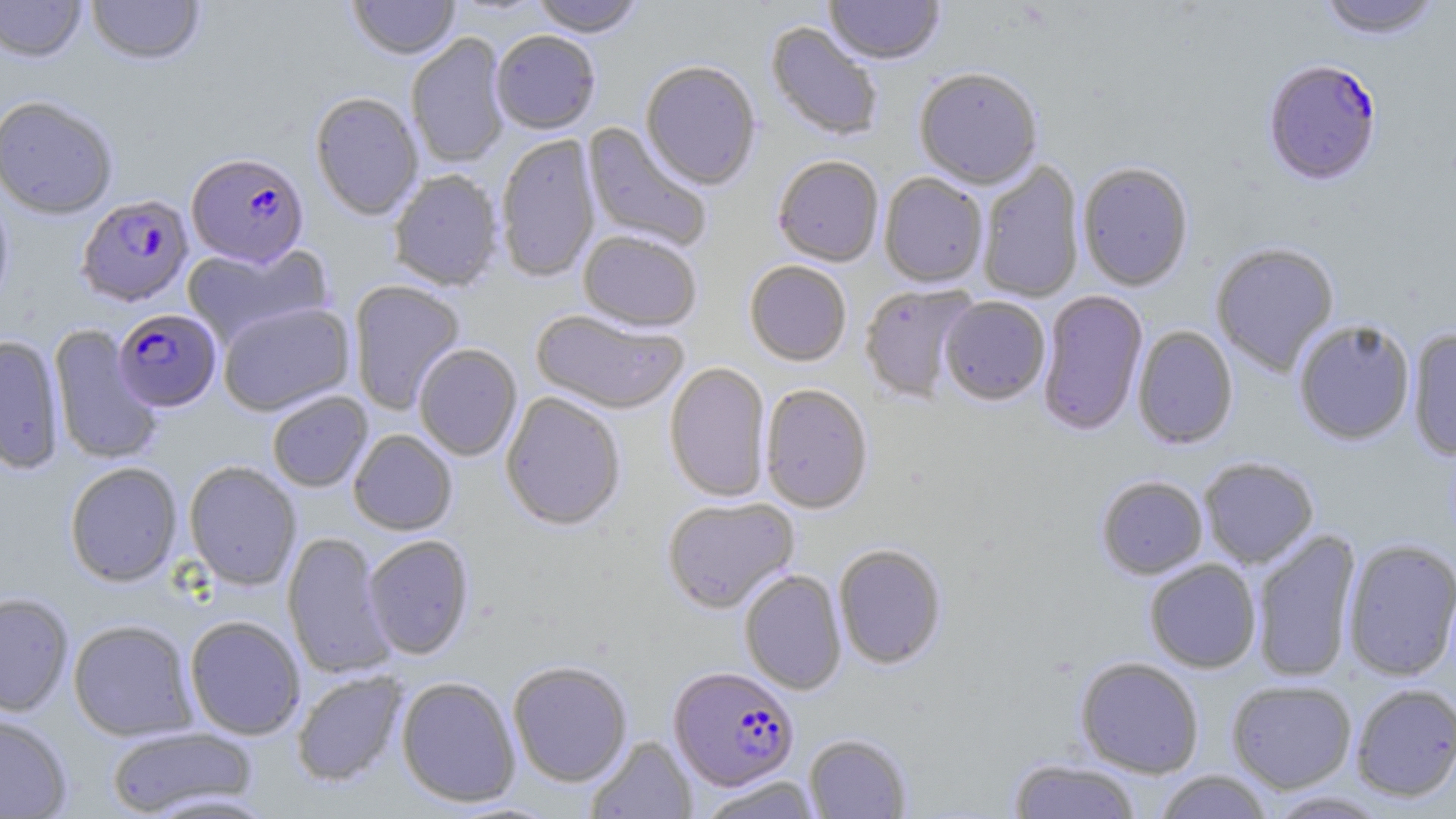 Approximate bounding boxes as (x1, y1, x2, y2) in pixels. Uninfected red blood cell locations: (0, 0, 88, 62), (85, 0, 205, 67), (347, 0, 461, 60), (530, 0, 646, 37), (825, 0, 944, 66), (1315, 0, 1445, 40), (765, 21, 884, 142), (490, 30, 601, 135), (406, 33, 510, 169), (640, 61, 761, 190), (913, 69, 1043, 189), (310, 92, 423, 221), (0, 94, 120, 220), (582, 122, 712, 253), (495, 134, 600, 283), (773, 156, 884, 267), (977, 159, 1084, 303), (1077, 161, 1194, 291), (388, 169, 504, 291), (879, 173, 988, 287), (0, 182, 14, 319), (578, 230, 702, 333), (1211, 242, 1340, 376), (182, 243, 332, 348), (744, 260, 852, 366), (348, 280, 466, 415), (859, 283, 977, 403), (1037, 290, 1148, 435), (939, 296, 1051, 405), (217, 301, 355, 415), (528, 309, 689, 416), (1293, 318, 1416, 445), (48, 325, 162, 465), (1132, 325, 1238, 450), (1407, 328, 1456, 462), (0, 335, 66, 474), (414, 344, 522, 461), (664, 362, 771, 503), (759, 383, 873, 514), (267, 391, 373, 492), (500, 391, 626, 530), (348, 429, 457, 535), (1198, 456, 1319, 567), (64, 461, 183, 587), (183, 461, 302, 590), (1096, 475, 1208, 579), (662, 496, 799, 613), (1250, 528, 1362, 683), (282, 531, 396, 680), (363, 535, 474, 660), (1342, 538, 1456, 681), (833, 543, 947, 670), (1144, 559, 1261, 673), (739, 569, 847, 695), (0, 592, 74, 716), (184, 615, 305, 740), (68, 619, 198, 742), (1075, 656, 1204, 778), (508, 661, 633, 786), (292, 670, 407, 787), (396, 676, 521, 808), (1226, 680, 1357, 793), (1350, 683, 1456, 802), (0, 714, 72, 818), (106, 725, 259, 816), (804, 733, 912, 818), (585, 735, 697, 819), (1008, 758, 1142, 818), (1153, 770, 1274, 819), (695, 776, 825, 819), (1264, 791, 1392, 818). Plasmodium falciparum-infected red blood cell locations: (1262, 58, 1383, 187), (186, 152, 310, 268), (76, 194, 194, 307), (113, 308, 221, 411), (668, 665, 799, 791). Slide-level diagnosis: Plasmodium falciparum. Optical microscopy. Single field of view. May-Grünwald-Giemsa stain. Image is 1456×819 pixels. 1000x magnification. Thin blood smear.